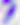
Toxoplasma gondii is shown. Photomicrograph. 400x magnification.